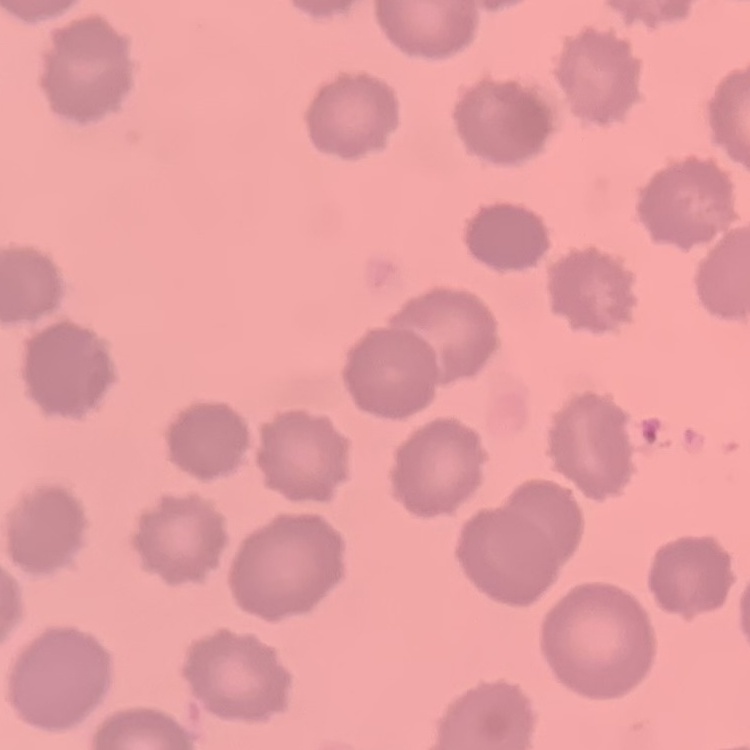

{
  "erythrocyte_morphology": "no rouleaux formation",
  "image_type": "one tile cut from a larger photomicrograph",
  "preparation": "thin blood smear",
  "stain": "Field's or Giemsa"
}